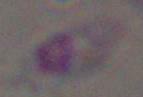 Micrograph. Toxoplasma gondii is shown. Captured at 1000x magnification.